Classify this cell by malaria status.
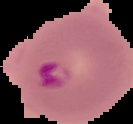

It is parasitized.

Summary:
  - Image size: 133×124 pixels
  - Preparation: thin blood smear
  - Image type: cell region segmented out of the field of view; surrounding area masked to black